Locate and identify every blood parasite.
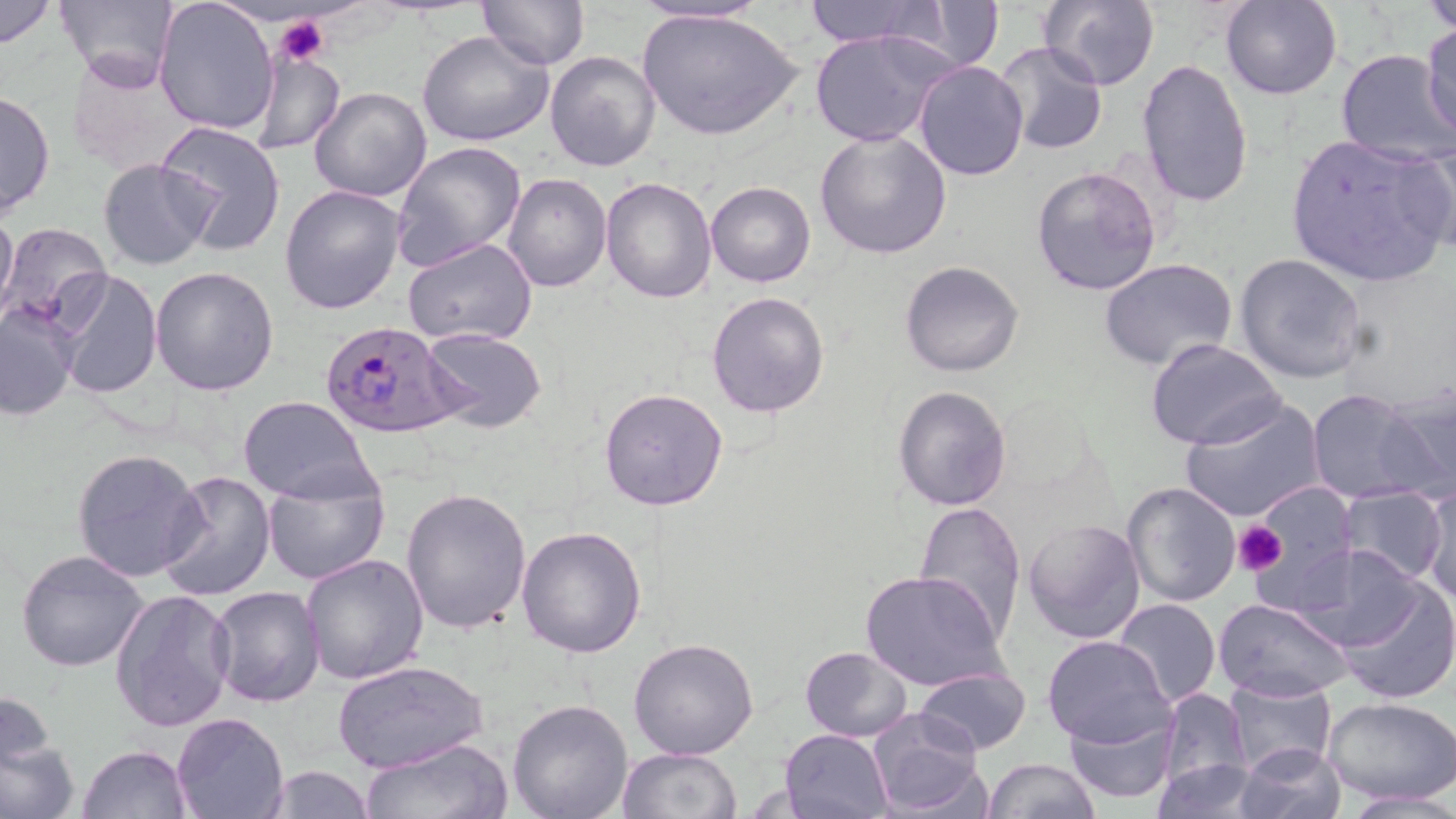
Approximate bounding boxes as (x1, y1, x2, y2) in pixels.
Plasmodium falciparum-infected red blood cells: (321, 322, 460, 438).
No Plasmodium ovale, Plasmodium malariae, Plasmodium vivax, Babesia divergens, or Trypanosoma brucei observed.

Platelet locations: (276, 15, 331, 67), (1233, 520, 1288, 576). Uninfected red blood cell locations: (0, 0, 58, 50), (56, 0, 180, 93), (152, 0, 279, 135), (476, 0, 588, 70), (801, 0, 945, 48), (900, 0, 1004, 71), (1039, 0, 1160, 88), (1220, 0, 1343, 100), (1422, 0, 1456, 34), (630, 2, 773, 26), (637, 7, 804, 144), (271, 16, 340, 64), (1421, 23, 1456, 143), (809, 29, 955, 149), (418, 30, 552, 147), (989, 42, 1110, 156), (436, 45, 658, 155), (66, 49, 194, 176), (249, 49, 345, 157), (545, 50, 663, 172), (1335, 50, 1455, 164), (1136, 58, 1255, 206), (914, 61, 1029, 183), (0, 87, 55, 218), (309, 87, 433, 203), (156, 121, 286, 256), (813, 129, 954, 260), (1285, 134, 1453, 287), (1404, 135, 1456, 260), (391, 141, 528, 272), (99, 158, 215, 270), (1030, 166, 1162, 297), (502, 174, 613, 293), (601, 176, 717, 303), (706, 180, 815, 287), (279, 184, 405, 316), (0, 205, 18, 327), (1, 222, 114, 334), (402, 238, 537, 348), (1234, 252, 1368, 383), (1098, 256, 1237, 370), (899, 260, 1024, 377), (52, 266, 163, 398), (149, 266, 279, 396), (706, 291, 830, 419), (0, 304, 78, 420), (421, 328, 547, 432), (1146, 338, 1285, 451), (1383, 379, 1455, 500), (892, 385, 1013, 511), (599, 388, 730, 512), (1307, 388, 1434, 506), (238, 395, 374, 502), (1178, 398, 1327, 523), (71, 447, 207, 582), (156, 470, 277, 602), (261, 474, 390, 586), (1121, 481, 1242, 608), (1245, 484, 1358, 607), (1419, 484, 1455, 601), (1338, 486, 1447, 585), (400, 488, 532, 634), (913, 499, 1026, 638), (1021, 518, 1146, 645), (516, 526, 648, 658), (1291, 542, 1428, 654), (16, 549, 150, 673), (300, 554, 431, 686), (860, 569, 1006, 690), (1334, 574, 1456, 705), (208, 586, 326, 707), (109, 587, 236, 732), (1112, 598, 1220, 709), (1212, 598, 1355, 705), (1042, 636, 1172, 748), (628, 637, 759, 759), (799, 646, 914, 742), (331, 659, 488, 772), (912, 665, 1031, 756), (1224, 674, 1338, 777), (0, 686, 63, 788), (1154, 686, 1254, 801), (1323, 696, 1456, 804), (507, 699, 635, 819), (1061, 701, 1180, 807), (867, 708, 984, 815), (172, 711, 288, 818), (0, 729, 79, 819), (778, 729, 895, 817), (359, 736, 514, 819), (1233, 741, 1347, 819), (78, 743, 194, 818), (618, 746, 741, 819), (982, 758, 1100, 819), (1151, 758, 1269, 817), (258, 763, 380, 819), (1337, 790, 1456, 817). Slide-level diagnosis: Plasmodium falciparum. Single field of view. May-Grünwald-Giemsa-stained preparation. Optical microscopy. Thin blood smear. Image is 1456×819 pixels. Captured at 1000x magnification.